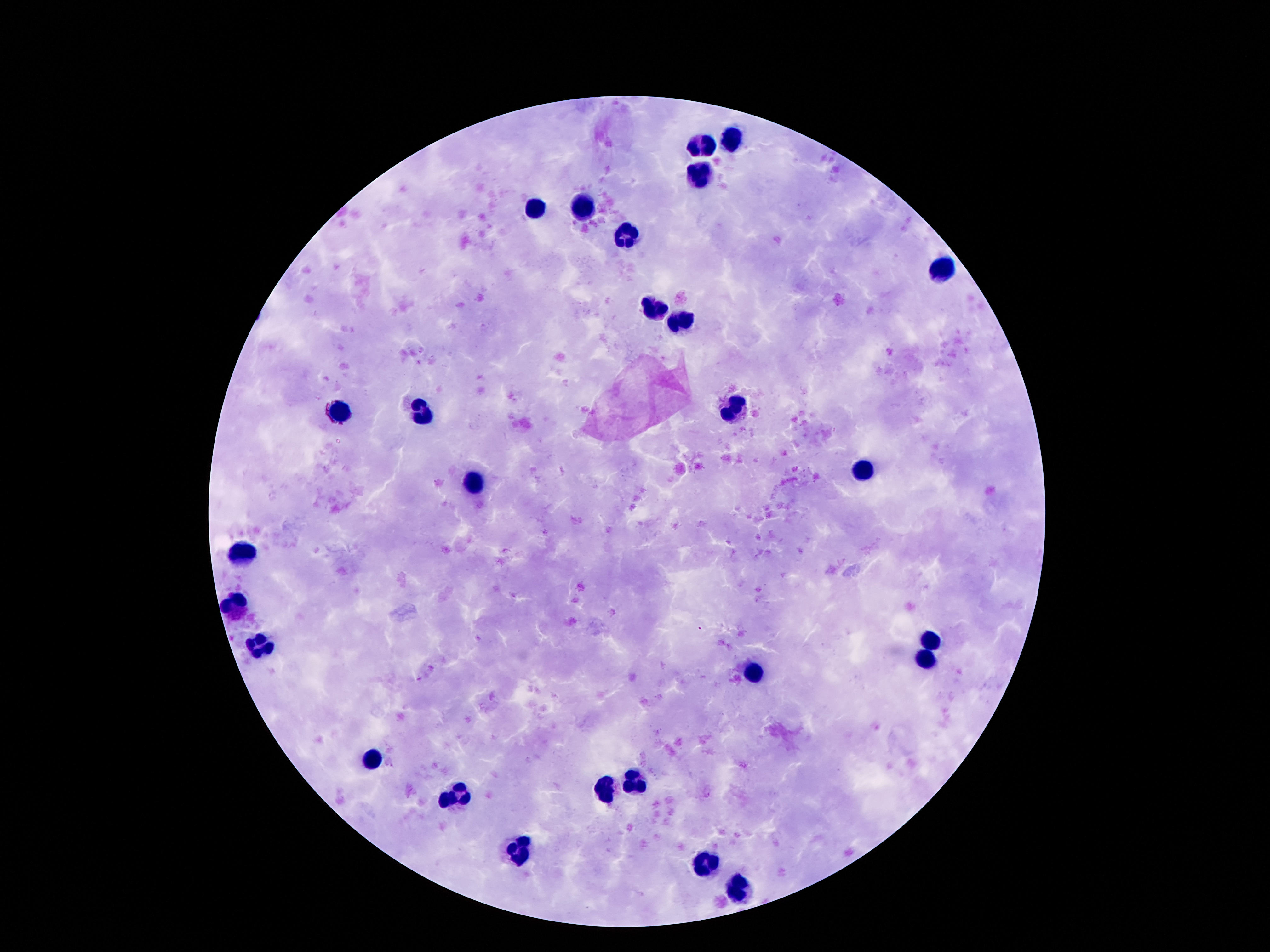
magnification = 100x
image size = 1270×952 pixels
patient malaria status = not infected
preparation = thick peripheral-blood smear
stain = Giemsa
capture = smartphone camera through the microscope eyepiece
field of view = one from this slide
leukocyte locations = approximate centers as [x, y] in pixels: [734, 136], [704, 145], [701, 173], [533, 206], [580, 206], [628, 233], [942, 268], [656, 307], [681, 318], [737, 401], [340, 408], [421, 410], [863, 469], [474, 480], [244, 547], [236, 603], [930, 640], [264, 642], [928, 654], [754, 673], [373, 756], [635, 777], [463, 788], [608, 789], [522, 851], [703, 862], [740, 888]